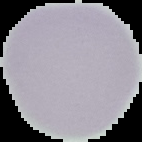
malaria status = uninfected
preparation = thin blood film
image size = 142×142 pixels
image type = segmented cell region with the area outside set to black